Assess this cell for malaria.
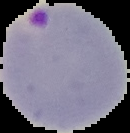
Parasitized.

Summary:
  - Image size: 130×133 pixels
  - Image type: segmented cell region with the area outside set to black
  - Preparation: thin blood smear